Give the extent of all Trypanosoma brucei.
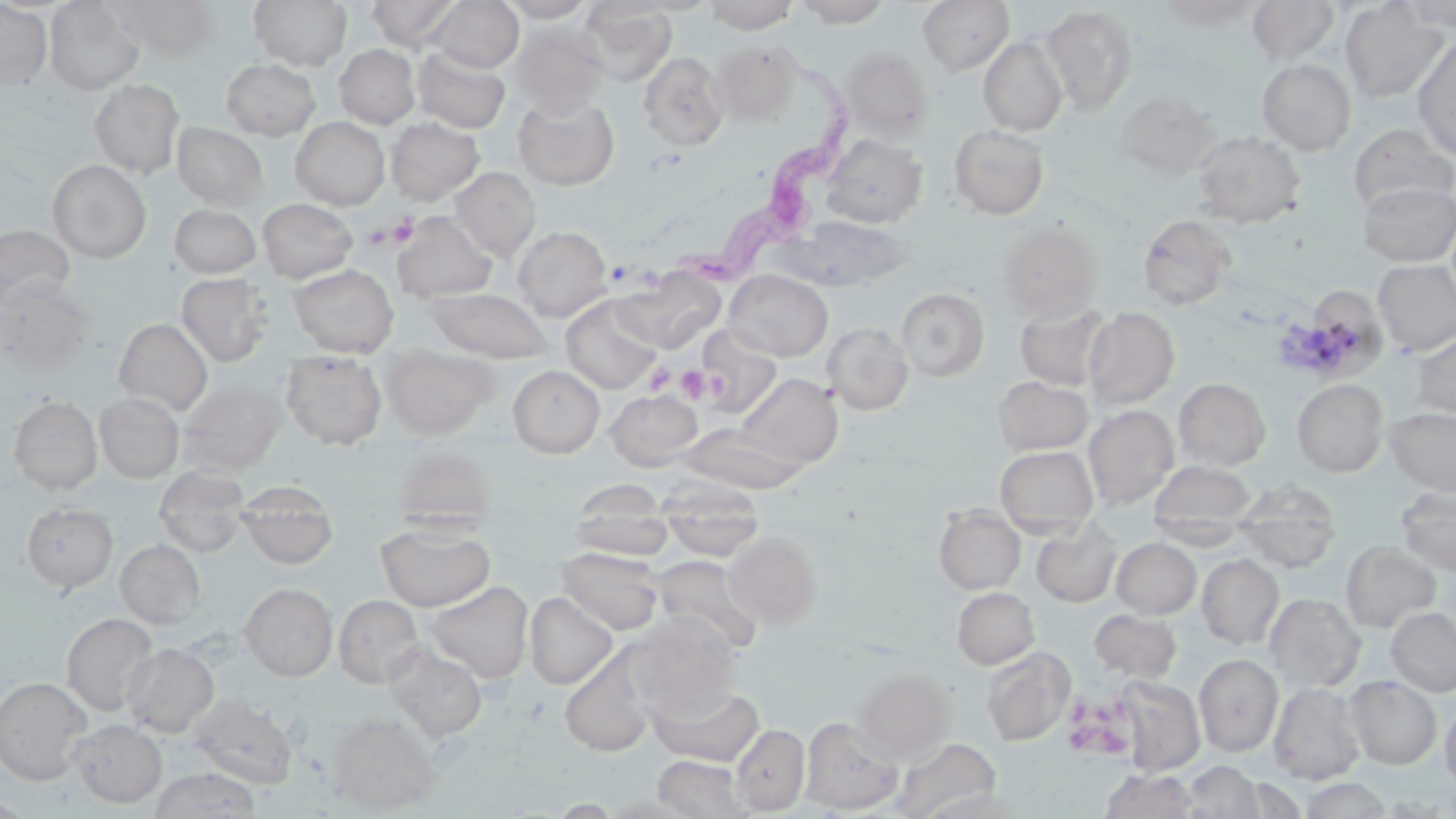
Approximate bounding boxes as [x1, y1, x2, y2] in pixels.
Trypanosoma brucei: [670, 42, 858, 293].

slide-level diagnosis = Trypanosoma brucei
image size = 1456×819 pixels
stain = May-Grünwald-Giemsa
uninfected red blood cell locations = approximate bounding boxes as [x1, y1, x2, y2] in pixels: [111, 0, 221, 59], [249, 0, 352, 70], [366, 0, 463, 50], [426, 0, 523, 73], [496, 0, 597, 22], [624, 0, 721, 15], [703, 0, 799, 34], [791, 0, 893, 27], [917, 0, 1014, 75], [1247, 0, 1340, 65], [44, 1, 144, 95], [1160, 1, 1261, 28], [1340, 1, 1448, 102], [1401, 1, 1456, 32], [0, 2, 53, 90], [579, 4, 676, 86], [1040, 5, 1139, 114], [509, 23, 608, 117], [978, 35, 1068, 136], [1412, 36, 1456, 159], [711, 41, 801, 124], [334, 44, 420, 129], [412, 45, 511, 133], [839, 47, 935, 142], [638, 51, 729, 151], [221, 58, 320, 140], [1257, 59, 1356, 155], [89, 79, 184, 178], [1114, 90, 1219, 179], [512, 93, 619, 191], [290, 117, 390, 210], [385, 117, 485, 205], [172, 122, 269, 209], [948, 124, 1049, 220], [1348, 124, 1456, 215], [1192, 131, 1306, 228], [821, 133, 928, 228], [47, 159, 151, 263], [450, 167, 540, 260], [1358, 182, 1456, 267], [257, 198, 357, 283], [169, 204, 261, 278], [392, 212, 497, 304], [1138, 214, 1236, 309], [781, 215, 914, 291], [996, 221, 1102, 321], [0, 224, 74, 307], [512, 226, 611, 321], [1373, 259, 1456, 356], [289, 264, 399, 357], [616, 269, 724, 353], [724, 270, 833, 361], [177, 273, 272, 366], [1, 277, 96, 375], [424, 287, 554, 363], [897, 288, 989, 381], [1312, 289, 1389, 380], [561, 295, 662, 394], [1015, 301, 1113, 390], [1083, 307, 1179, 410], [113, 318, 212, 415], [822, 322, 914, 414], [696, 326, 783, 418], [1412, 333, 1456, 417], [381, 344, 498, 439], [280, 350, 387, 450], [508, 365, 605, 458], [735, 373, 843, 470], [993, 376, 1093, 455], [1174, 378, 1270, 470], [177, 379, 286, 474], [1292, 379, 1388, 476], [605, 390, 703, 470], [95, 392, 184, 483], [8, 396, 102, 495], [1084, 405, 1179, 508], [1385, 407, 1456, 495], [677, 424, 805, 494], [393, 443, 497, 532], [995, 444, 1098, 535], [1151, 460, 1255, 541], [154, 465, 250, 558], [658, 479, 763, 562], [1234, 480, 1341, 573], [237, 481, 338, 570], [1396, 487, 1456, 577], [571, 490, 673, 562], [21, 502, 117, 593], [934, 505, 1025, 594], [1031, 519, 1122, 607], [376, 522, 494, 612], [723, 531, 821, 628], [1111, 537, 1201, 619], [115, 539, 205, 628], [1341, 541, 1442, 632], [557, 547, 664, 635], [1196, 553, 1284, 649], [650, 555, 762, 655], [424, 581, 533, 684], [239, 583, 337, 681], [952, 587, 1039, 669], [525, 592, 618, 689], [1264, 592, 1365, 691], [334, 594, 423, 688], [1386, 607, 1456, 696], [1090, 609, 1181, 683], [62, 613, 160, 718], [629, 614, 740, 715], [122, 642, 218, 737], [385, 644, 488, 741], [982, 647, 1075, 746], [560, 651, 657, 757], [1194, 654, 1283, 757], [851, 668, 954, 763], [1345, 675, 1441, 768], [0, 676, 93, 785], [1114, 676, 1205, 775], [1269, 681, 1366, 784], [647, 682, 764, 766], [188, 694, 299, 790], [1440, 699, 1456, 791], [326, 712, 442, 812], [800, 716, 903, 814], [70, 719, 166, 807], [732, 724, 810, 814], [891, 738, 1002, 819], [652, 755, 754, 818], [1183, 760, 1269, 818], [149, 767, 262, 818], [1099, 767, 1199, 818], [1299, 777, 1393, 818], [0, 794, 35, 818]
magnification = 1000x
preparation = thin blood smear
modality = light microscopy
platelet locations = approximate bounding boxes as [x1, y1, x2, y2] in pixels: [387, 212, 419, 246], [364, 223, 395, 250], [645, 361, 675, 394], [677, 365, 710, 402], [702, 365, 728, 403], [1065, 693, 1140, 761]
field of view = one of a larger specimen